Identify the cell.
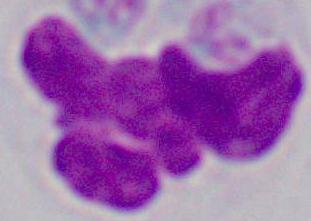
A leukocyte.

1000x magnification. Micrograph.